Locate every malaria parasite by life-cycle stage, and every leukocyte.
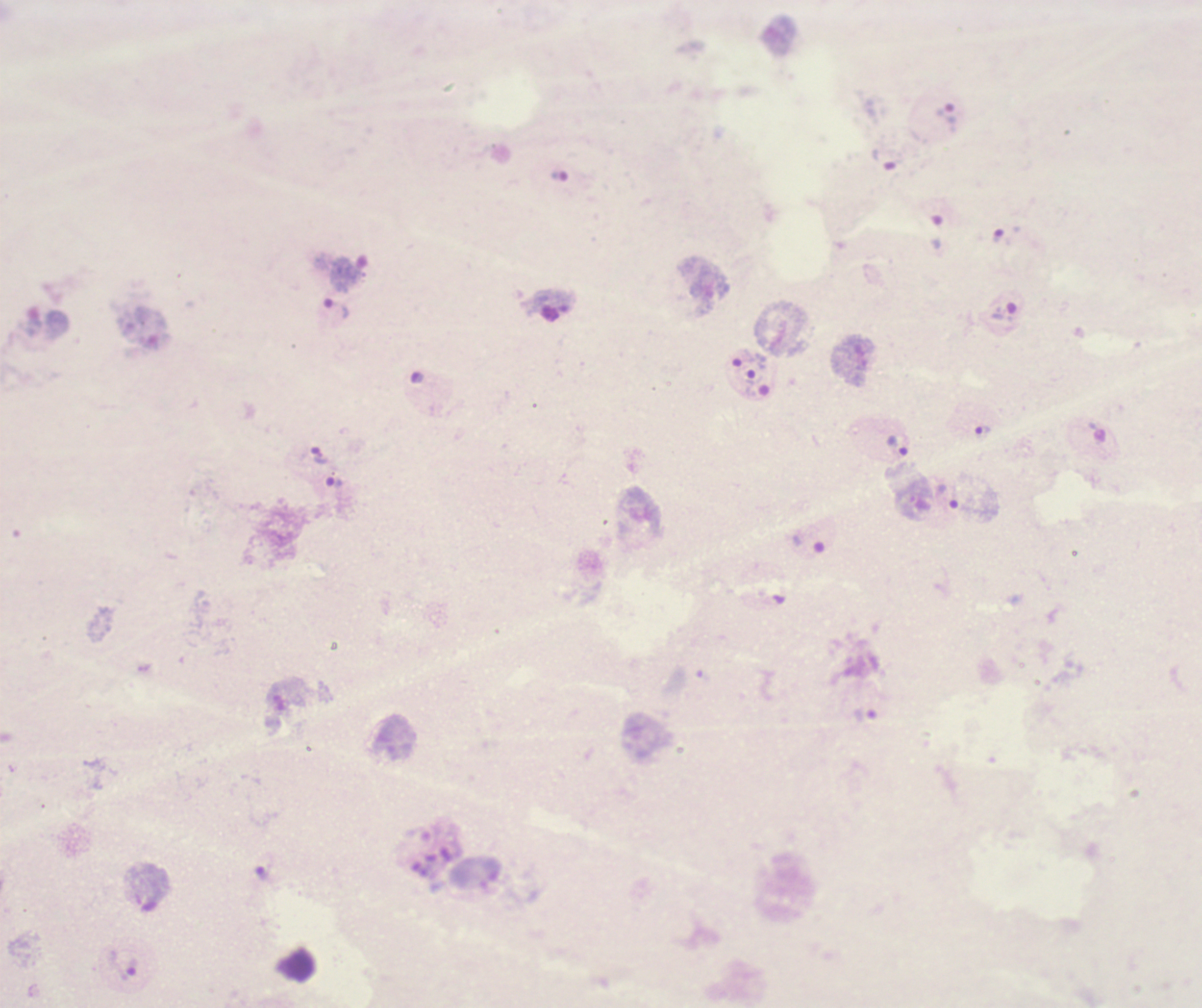
Approximate centers as (x, y) in pixels.
Trophozoites: (945, 114), (883, 161), (350, 272), (336, 310), (1003, 313), (745, 358), (983, 430), (898, 446), (319, 456), (335, 483), (264, 872), (123, 963).
No schizont or gametocyte forms observed.
No leukocytes visible.

{
  "field_of_view": "one from this slide",
  "preparation": "thick blood smear",
  "image_size": "1202×1008 pixels",
  "background_quality": "poor",
  "magnification": "100x",
  "coloration_quality": "bad",
  "stain": "Romanowsky",
  "context": "previously used in a real diagnosis"
}